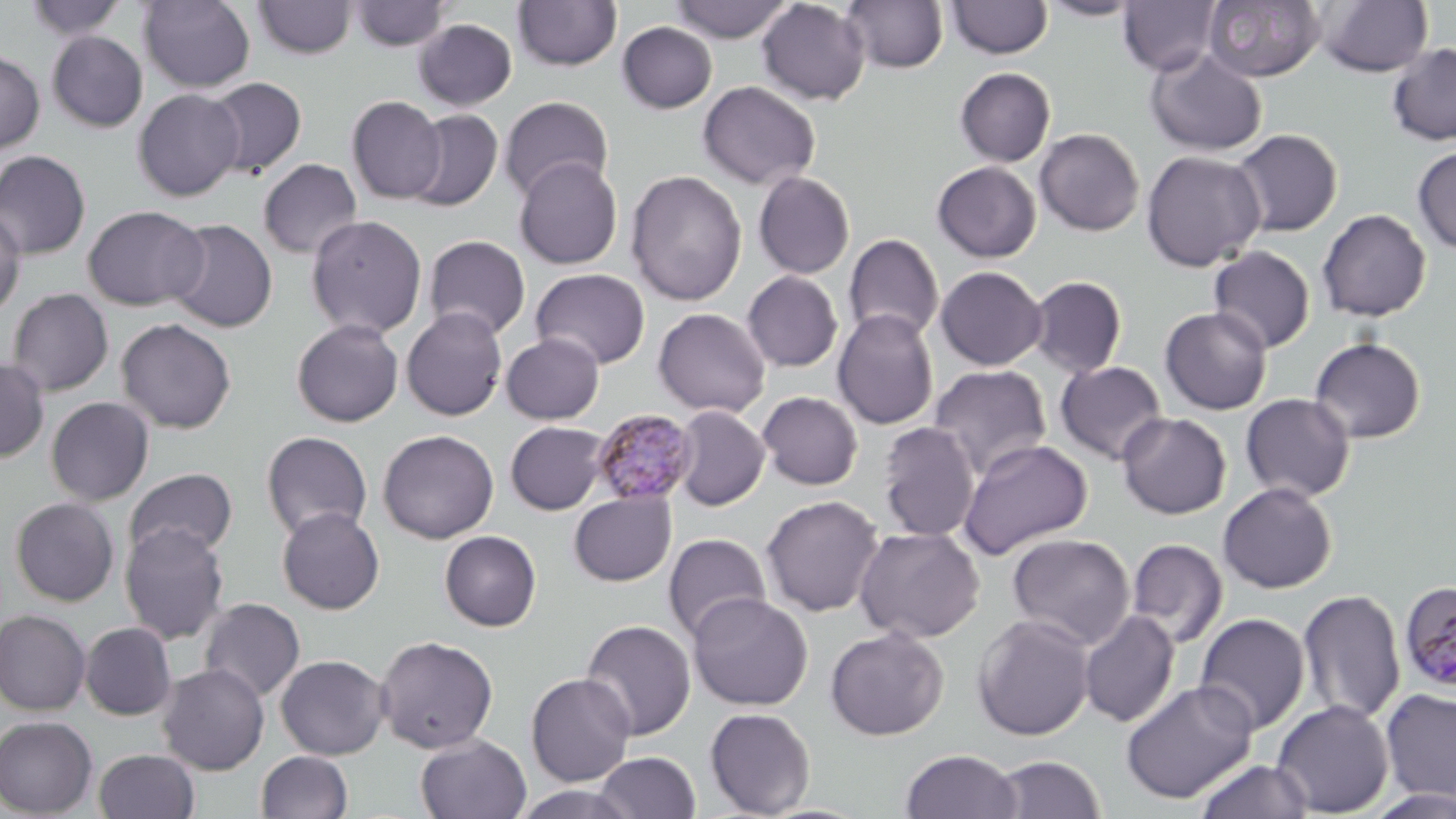

Approximate bounding boxes as [x1, y1, x2, y2] in pixels. Plasmodium malariae-infected red blood cell locations: [590, 407, 698, 506], [1399, 579, 1456, 692]. Uninfected red blood cell locations: [25, 0, 129, 40], [254, 0, 357, 58], [348, 0, 453, 52], [671, 0, 793, 42], [757, 0, 870, 105], [842, 0, 949, 73], [947, 0, 1053, 59], [1039, 0, 1146, 20], [1117, 0, 1222, 76], [1317, 0, 1432, 77], [138, 1, 255, 92], [513, 1, 622, 71], [1202, 1, 1325, 83], [413, 19, 517, 110], [617, 22, 718, 113], [47, 31, 147, 132], [1387, 43, 1456, 145], [1145, 49, 1268, 157], [0, 50, 44, 154], [954, 67, 1056, 166], [205, 77, 307, 178], [698, 81, 820, 190], [133, 89, 244, 201], [499, 95, 614, 202], [347, 96, 446, 204], [405, 108, 503, 211], [1034, 128, 1144, 236], [1231, 129, 1342, 236], [1412, 145, 1456, 254], [0, 150, 91, 259], [1141, 150, 1266, 271], [514, 157, 623, 269], [258, 159, 362, 259], [932, 161, 1042, 262], [625, 170, 748, 306], [753, 171, 856, 279], [83, 205, 208, 311], [0, 207, 26, 317], [1317, 208, 1431, 321], [306, 215, 428, 339], [166, 219, 277, 333], [843, 234, 944, 343], [423, 235, 531, 339], [1207, 246, 1316, 353], [935, 266, 1047, 370], [530, 268, 651, 369], [741, 271, 844, 372], [1028, 275, 1128, 378], [6, 287, 113, 396], [1159, 306, 1272, 415], [401, 307, 508, 421], [652, 307, 771, 417], [832, 309, 939, 430], [116, 318, 236, 434], [291, 318, 404, 427], [501, 333, 604, 424], [1309, 336, 1427, 443], [0, 357, 49, 463], [1055, 361, 1168, 465], [927, 364, 1052, 479], [757, 391, 863, 490], [1240, 393, 1356, 502], [45, 396, 153, 506], [671, 406, 770, 511], [1117, 412, 1231, 519], [505, 421, 610, 514], [877, 421, 981, 542], [377, 429, 499, 544], [260, 431, 372, 541], [957, 438, 1093, 560], [124, 468, 238, 562], [1218, 482, 1337, 594], [568, 489, 677, 587], [761, 495, 883, 617], [10, 497, 119, 606], [277, 507, 385, 615], [120, 522, 229, 644], [854, 526, 984, 644], [439, 530, 542, 631], [663, 533, 771, 643], [1007, 533, 1135, 649], [1126, 538, 1228, 649], [1297, 589, 1406, 725], [687, 592, 813, 710], [199, 597, 306, 703], [0, 610, 91, 716], [1079, 610, 1180, 728], [1193, 613, 1310, 736], [972, 615, 1095, 741], [580, 619, 697, 740], [81, 622, 176, 720], [825, 627, 948, 740], [375, 635, 499, 753], [275, 654, 390, 760], [157, 663, 269, 775], [525, 672, 636, 787], [1120, 679, 1258, 804], [1380, 689, 1456, 803], [1272, 700, 1394, 817], [704, 707, 816, 817], [0, 715, 98, 818], [415, 734, 532, 819], [93, 749, 200, 819], [900, 749, 1022, 819], [256, 750, 353, 819], [592, 751, 701, 819], [992, 755, 1106, 818], [1193, 758, 1315, 819], [510, 784, 644, 819], [1362, 786, 1456, 818]. Slide-level diagnosis: Plasmodium malariae. Optical microscopy. Thin blood film. May-Grünwald-Giemsa stain. Single field of view. Image is 1456×819 pixels. 1000x magnification.